Identify the cell.
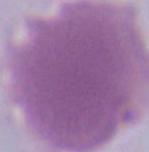
This is an erythrocyte.

Summary:
  - Modality: photomicrograph
  - Magnification: 1000x